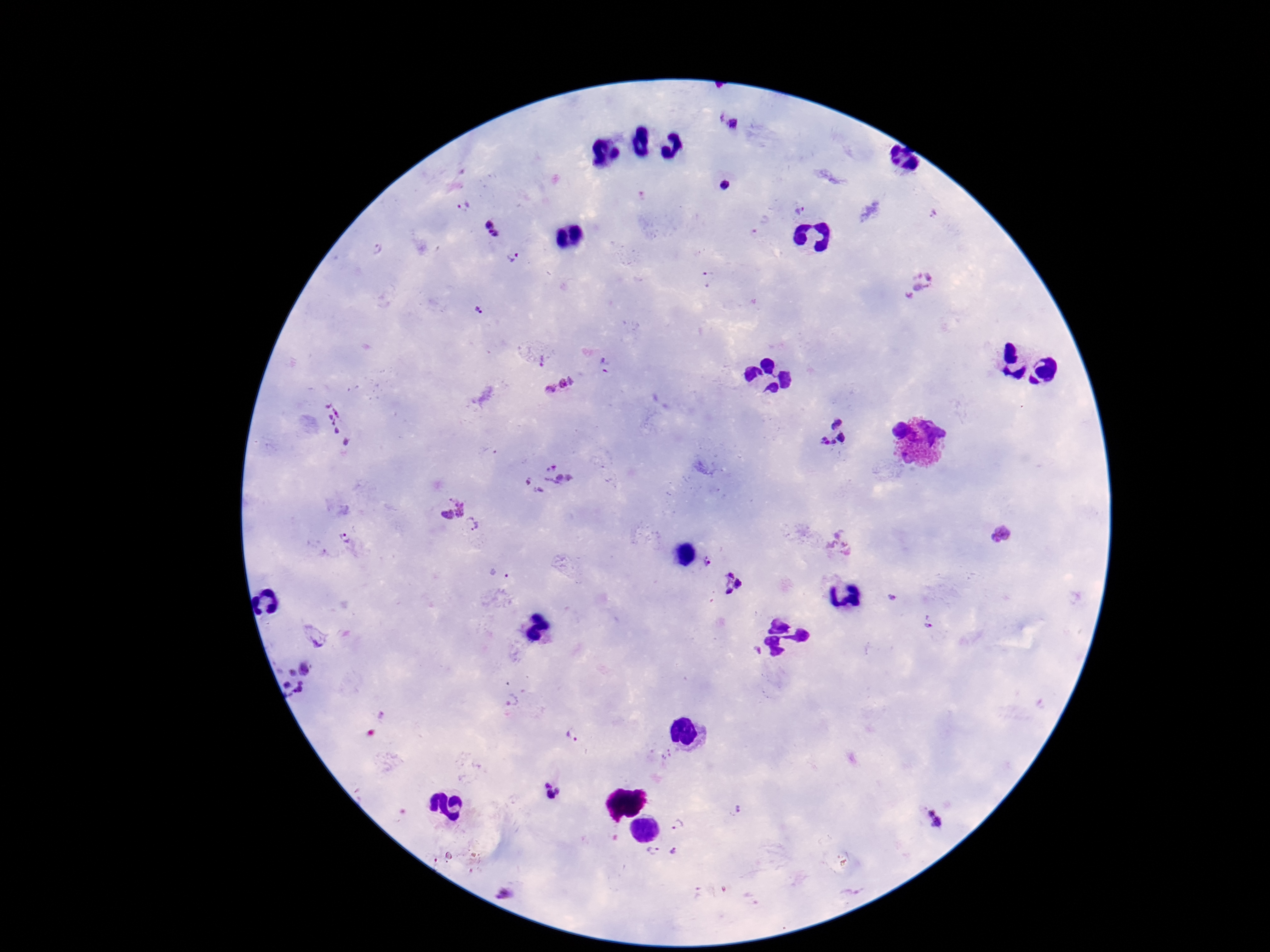

{
  "plasmodium_parasite_locations": "approximate centers as {x, y} in pixels: {727, 123}, {724, 183}, {464, 205}, {801, 211}, {931, 215}, {491, 229}, {378, 249}, {513, 257}, {708, 279}, {917, 287}, {480, 310}, {541, 360}, {605, 366}, {560, 388}, {335, 426}, {832, 434}, {548, 479}, {449, 506}, {472, 524}, {346, 540}, {707, 560}, {499, 572}, {732, 582}, {893, 596}, {930, 622}, {318, 637}, {293, 678}, {514, 701}, {572, 737}, {552, 792}, {736, 810}, {938, 818}, {678, 823}, {674, 852}, {652, 853}, {505, 892}",
  "preparation": "thick blood film",
  "image_size": "1270×952 pixels",
  "field_of_view": "single",
  "capture": "smartphone camera through the microscope eyepiece",
  "magnification": "100x",
  "stain": "Giemsa",
  "patient_malaria_status": "infected"
}